Report the malaria status of this cell.
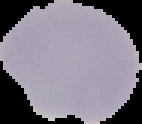

Uninfected.

preparation: thin blood smear
image_size: 142×124 pixels
image_type: segmented cell region with the area outside set to black